Assess this cell for malaria.
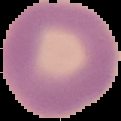

It is uninfected.

Summary:
  - Preparation: thin blood film
  - Image size: 121×121 pixels
  - Image type: cell region segmented out of the field of view; surrounding area masked to black